Name the cell type shown.
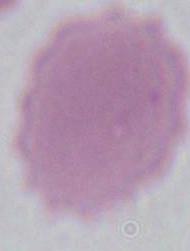

This is an erythrocyte.

Captured at 1000x magnification. Micrograph.